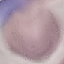

Result: negative for malaria parasites. Giemsa stain. Thin smear of blood. Cell patch, automatically extracted from a larger field of view and resized to 64 × 64 pixels. Acquired by smartphone through the microscope eyepiece.